Name the parasite shown.
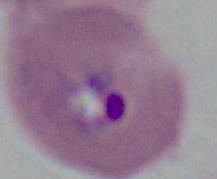

This is Plasmodium.

Summary:
  - Modality: photomicrograph
  - Magnification: 400x or 1000x